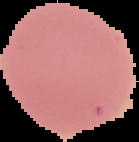

Summary:
  - Result: no malaria parasites seen
  - Image type: cell region segmented out of the field of view; surrounding area masked to black
  - Image size: 139×142 pixels
  - Preparation: thin blood film